Outline each Plasmodium falciparum-infected red blood cell.
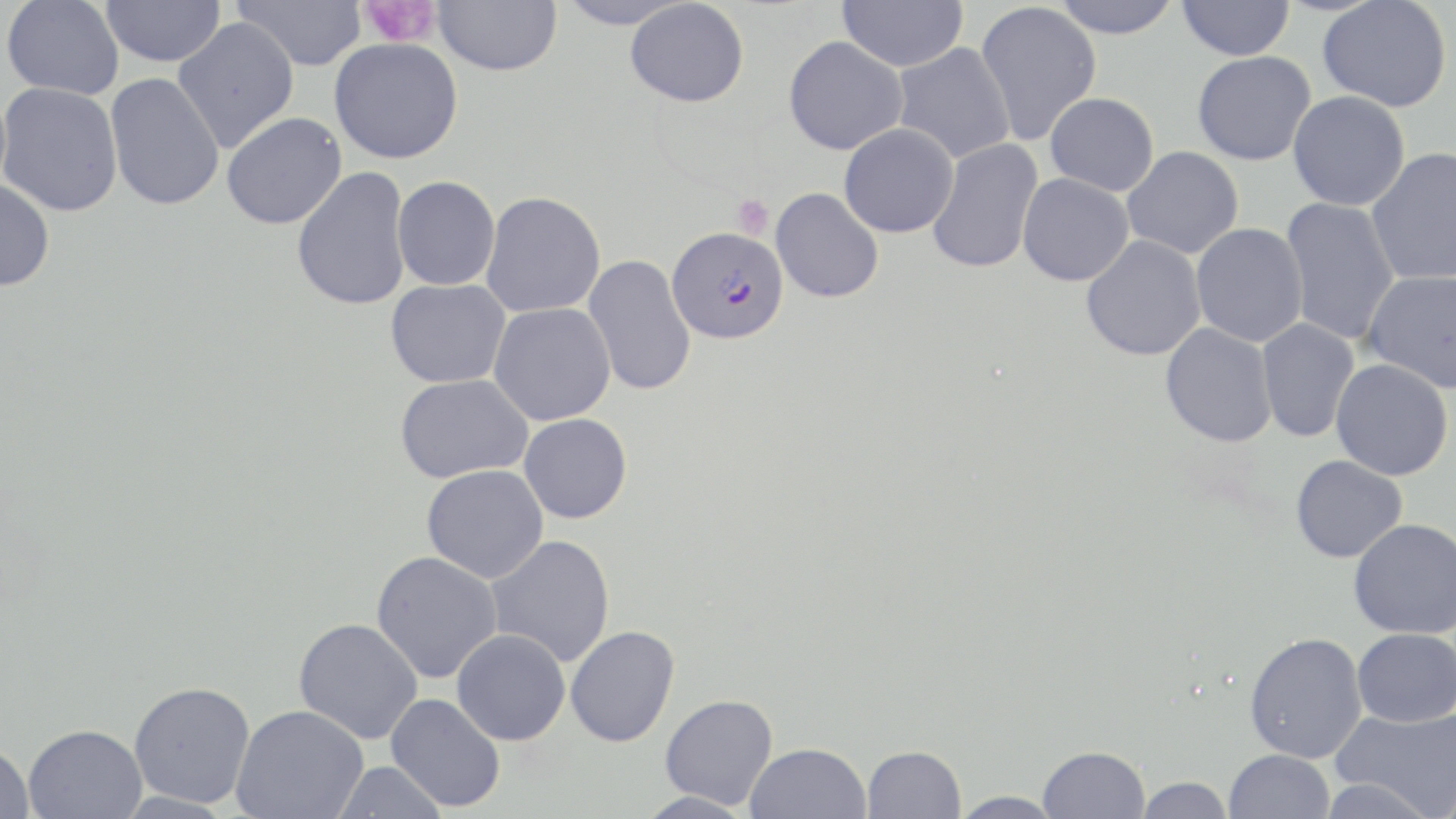
Approximate bounding boxes as [x1, y1, x2, y2] in pixels.
Plasmodium falciparum-infected red blood cells: [667, 226, 788, 344].

slide-level diagnosis = Plasmodium falciparum
stain = May-Grünwald-Giemsa
platelet locations = approximate bounding boxes as [x1, y1, x2, y2] in pixels: [358, 0, 441, 48], [731, 194, 774, 240]
image size = 1456×819 pixels
uninfected red blood cell locations = approximate bounding boxes as [x1, y1, x2, y2] in pixels: [2, 0, 124, 99], [100, 0, 225, 67], [233, 0, 366, 71], [433, 0, 562, 76], [555, 0, 689, 29], [837, 0, 968, 72], [1050, 0, 1183, 38], [1178, 0, 1294, 61], [1317, 0, 1452, 112], [626, 1, 748, 107], [975, 2, 1102, 146], [173, 17, 299, 152], [783, 36, 908, 155], [329, 38, 463, 164], [891, 43, 1015, 164], [1192, 51, 1316, 165], [105, 73, 225, 211], [0, 83, 123, 217], [1288, 90, 1410, 211], [1045, 92, 1159, 196], [221, 112, 346, 229], [839, 123, 958, 238], [926, 137, 1044, 274], [1122, 146, 1244, 260], [1365, 146, 1456, 285], [292, 166, 412, 311], [1017, 173, 1134, 286], [392, 175, 500, 290], [0, 178, 56, 292], [770, 188, 884, 304], [480, 192, 606, 318], [1280, 196, 1400, 345], [1191, 223, 1308, 348], [1080, 235, 1207, 361], [583, 255, 696, 396], [1363, 270, 1456, 393], [385, 279, 511, 388], [489, 302, 615, 425], [1256, 319, 1359, 443], [1160, 322, 1278, 448], [1331, 359, 1453, 480], [394, 374, 533, 483], [519, 413, 632, 523], [1290, 455, 1408, 563], [421, 464, 548, 583], [1349, 518, 1456, 639], [485, 535, 615, 667], [370, 550, 502, 684], [293, 617, 423, 744], [565, 625, 680, 747], [1352, 628, 1456, 727], [452, 629, 570, 745], [1244, 632, 1367, 763], [128, 680, 256, 808], [385, 693, 506, 812], [660, 693, 778, 809], [231, 705, 368, 819], [1331, 706, 1456, 815], [23, 723, 147, 818], [0, 740, 34, 818], [744, 742, 871, 819], [861, 745, 965, 819], [1038, 745, 1150, 819], [1225, 750, 1335, 819], [332, 760, 447, 818], [1317, 775, 1438, 819], [1134, 777, 1234, 819], [948, 790, 1066, 819]
preparation = thin blood film
modality = optical microscopy
magnification = 1000x
field of view = single